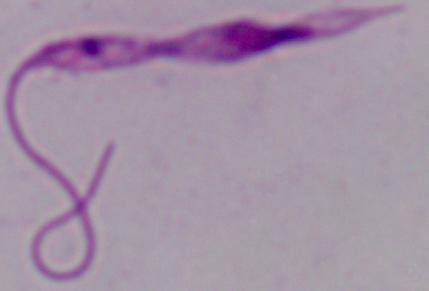

A Leishmania parasite is seen. Micrograph. Captured at 1000x magnification.